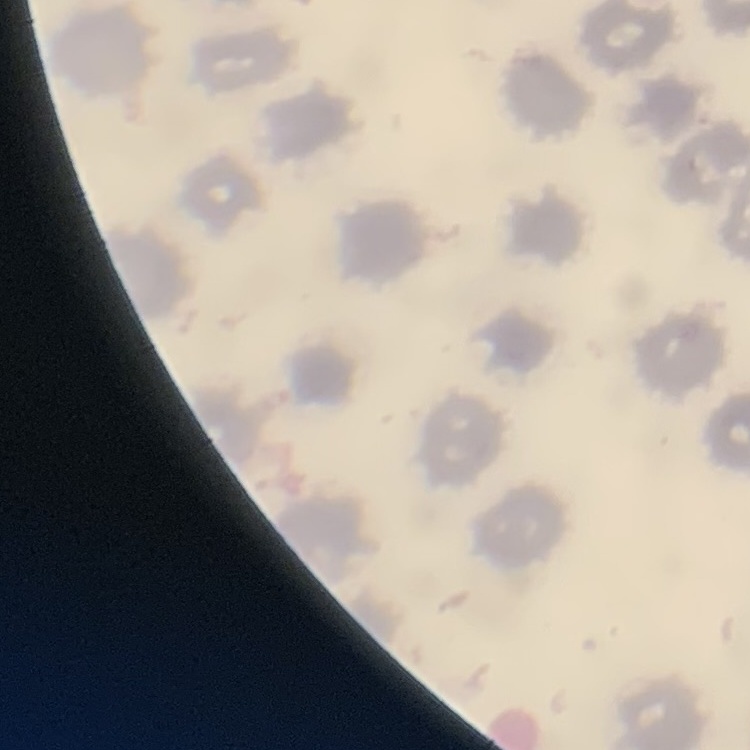
red blood cell morphology = no rouleaux formation
image type = square crop of a larger photomicrograph
stain = Field's or Giemsa
preparation = thin blood smear